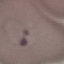

Summary:
  - Result: malaria parasites detected
  - Capture: smartphone camera at the microscope eyepiece
  - Stain: Giemsa
  - Preparation: thin blood smear
  - Image type: cell patch, automatically extracted from a larger field of view and resized to 64 × 64 pixels